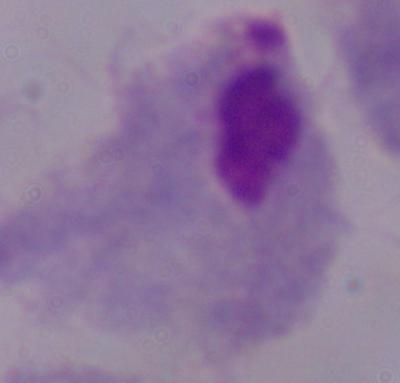
A trichomonad is shown. Captured at 1000x magnification. Photomicrograph.